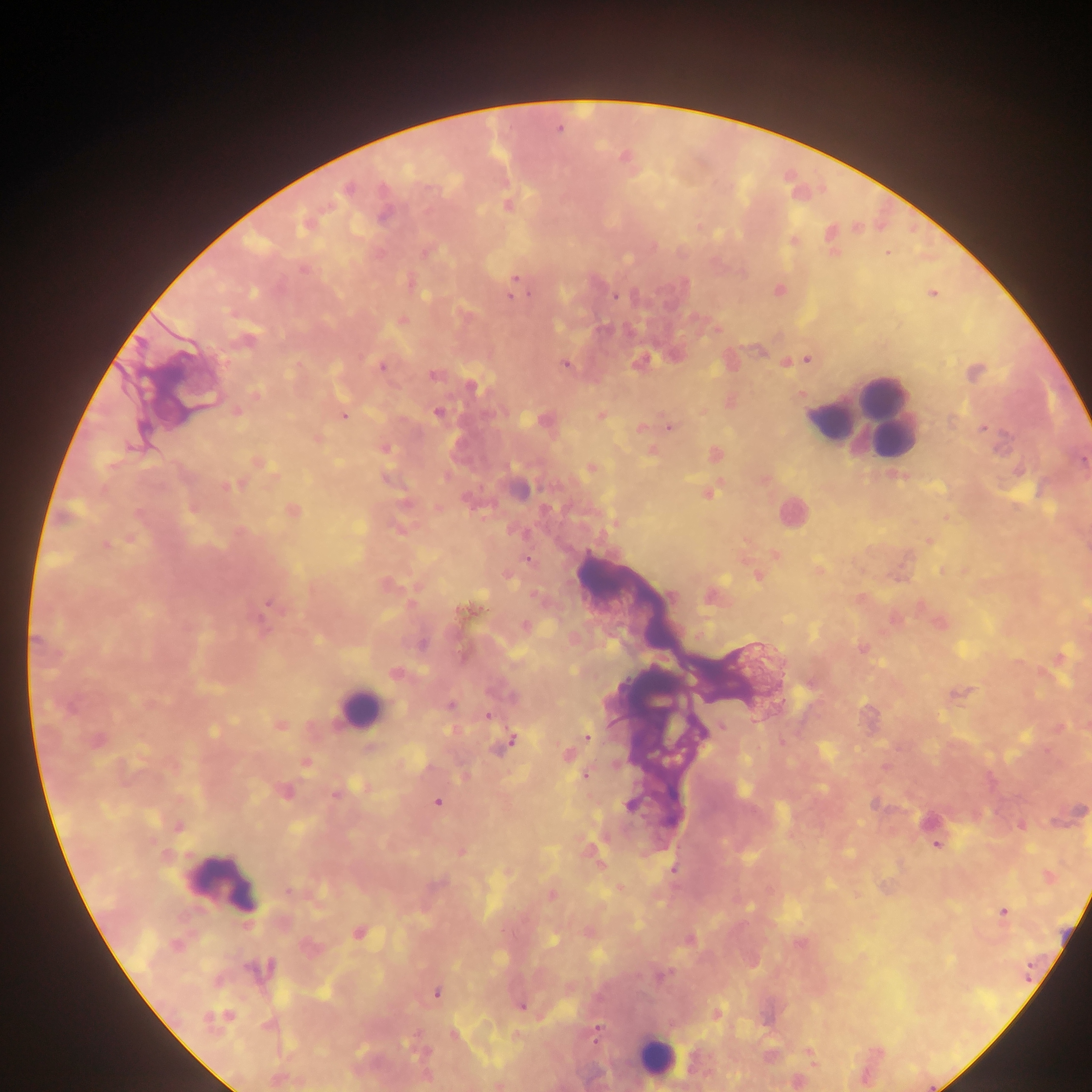

Approximate centers as (x, y) in pixels.
Summary:
  - Leukocyte locations: (883, 407), (846, 413), (863, 417), (793, 513), (358, 709), (221, 880), (656, 1058)
  - Malaria parasite locations: (560, 128), (626, 158), (348, 187), (508, 205), (307, 222), (830, 237), (793, 240), (426, 251), (887, 253), (302, 268), (515, 278), (409, 282), (778, 291), (932, 293), (615, 295), (511, 296), (402, 320), (717, 329), (245, 339), (759, 349), (808, 359), (640, 362), (785, 362), (565, 363), (381, 366), (974, 372), (433, 374), (471, 385), (255, 394), (801, 394), (729, 401), (236, 411), (438, 412), (703, 412), (600, 415), (343, 416), (545, 420), (951, 420), (668, 426), (639, 428), (983, 428), (316, 439), (384, 447), (651, 451), (714, 453), (257, 461), (591, 467), (1018, 470), (897, 474), (764, 480), (229, 485), (516, 488), (707, 494), (438, 509), (291, 511), (946, 517), (616, 523), (399, 528), (131, 538), (928, 540), (105, 545), (775, 555), (528, 559), (817, 570), (942, 570), (965, 571), (506, 574), (757, 575), (385, 583), (711, 596), (269, 604), (469, 609), (894, 619), (939, 623), (524, 625), (422, 644), (862, 649), (1058, 658), (395, 672), (957, 693), (513, 696), (450, 704), (488, 716), (279, 725), (721, 726), (1085, 726), (1058, 728), (587, 737), (96, 740), (511, 741), (370, 748), (567, 754), (306, 762), (885, 767), (586, 774), (464, 777), (365, 787), (284, 791), (336, 793), (437, 802), (875, 803), (1078, 811), (1020, 824), (178, 826), (936, 844), (460, 851), (597, 863), (673, 869), (507, 872), (1047, 877), (619, 887), (289, 892), (551, 895), (1003, 911), (357, 932), (588, 932), (688, 939), (799, 943), (176, 944), (309, 947), (265, 968), (661, 975), (436, 993), (521, 1005), (716, 1013), (218, 1019), (596, 1033), (453, 1034), (810, 1055), (277, 1079), (798, 1081), (499, 1084)
  - Field of view: single
  - Country: Ghana
  - Preparation: thick blood smear
  - Capture: mobile-phone photograph through a microscope
  - Image size: 1092×1092 pixels